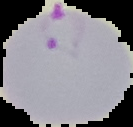

Cell region segmented out of the field of view; the surrounding area is masked to black. Result: malaria parasites identified. From a thin blood film. Image is 133×127 pixels.